Classify this cell by malaria status.
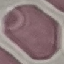

It is uninfected.

Summary:
  - Image type: cell patch, automatically extracted from a larger field of view and resized to 64 × 64 pixels
  - Stain: Giemsa
  - Preparation: thin smear
  - Capture: smartphone through the microscope eyepiece